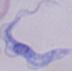 Micrograph. A trypanosome is seen. Captured at 1000x magnification.